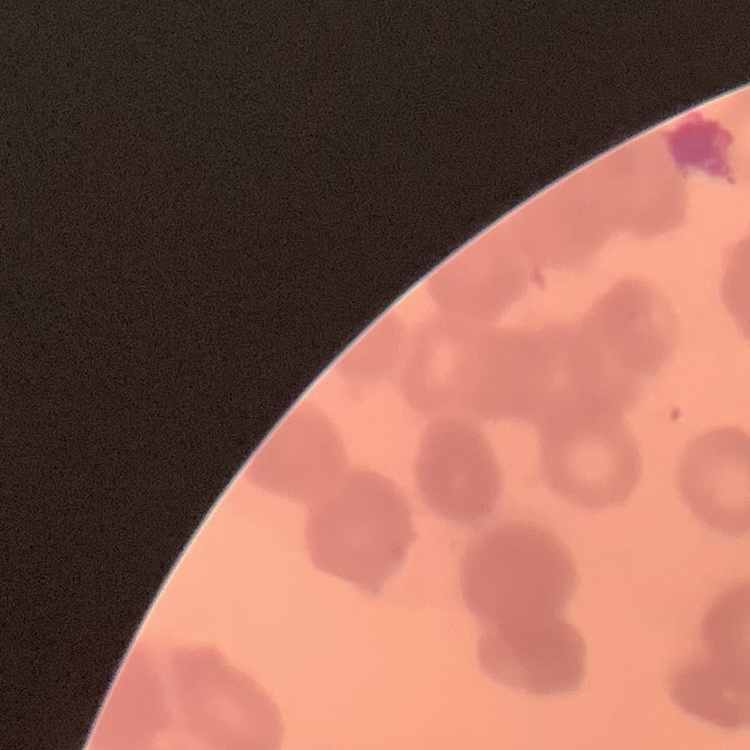
red blood cell morphology = rouleaux formation
image type = square crop of a larger photomicrograph
preparation = thin blood film
stain = Field's or Giemsa